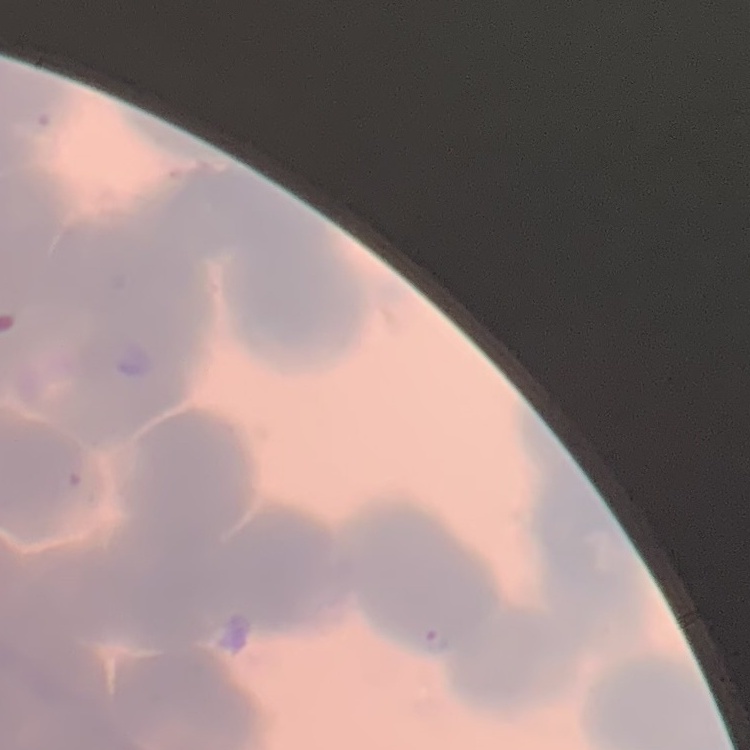

red_blood_cell_morphology: rouleaux formation
image_type: one tile cut from a larger photomicrograph
stain: Field's or Giemsa
preparation: thin peripheral smear